Report the malaria status of this cell.
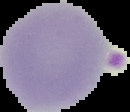
It is parasitized.

image size = 130×112 pixels
preparation = thin blood film
image type = segmented cell region with the area outside set to black